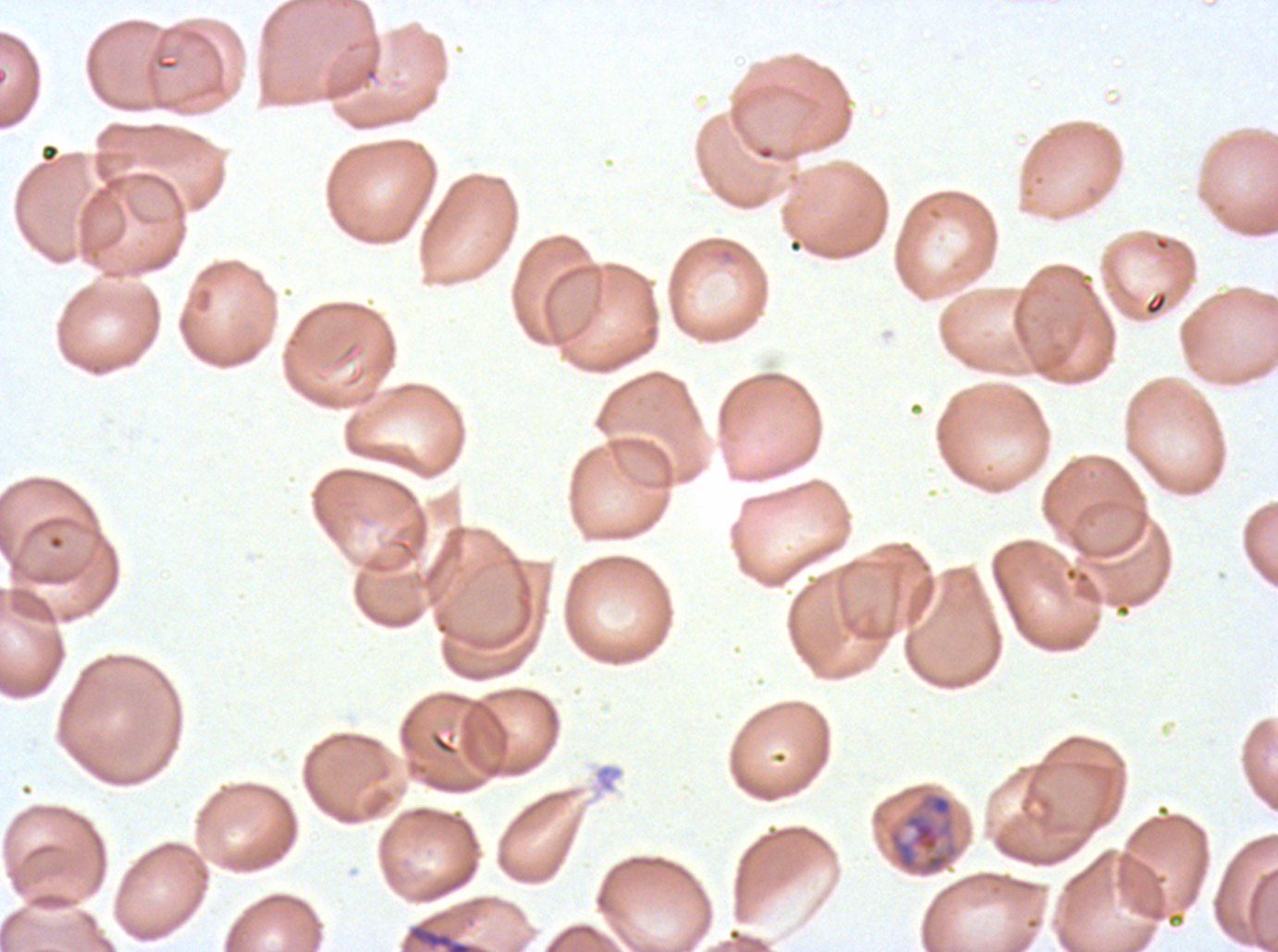 Approximate bounding boxes as (x1, y1, x2, y2) in pixels. Debris locations: (409, 924, 473, 951). Mid trophozoite locations: (886, 789, 960, 878). Giemsa-stained preparation. One sub-image of a larger composite. Ex-vivo P. falciparum culture from a patient in The Gambia, grown for 24 to 48 hours. Thin blood smear. Image is 1278×952 pixels.